Identify the parasite.
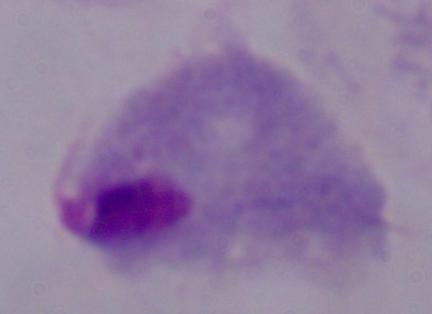

A trichomonad.

Summary:
  - Modality: photomicrograph
  - Magnification: 1000x